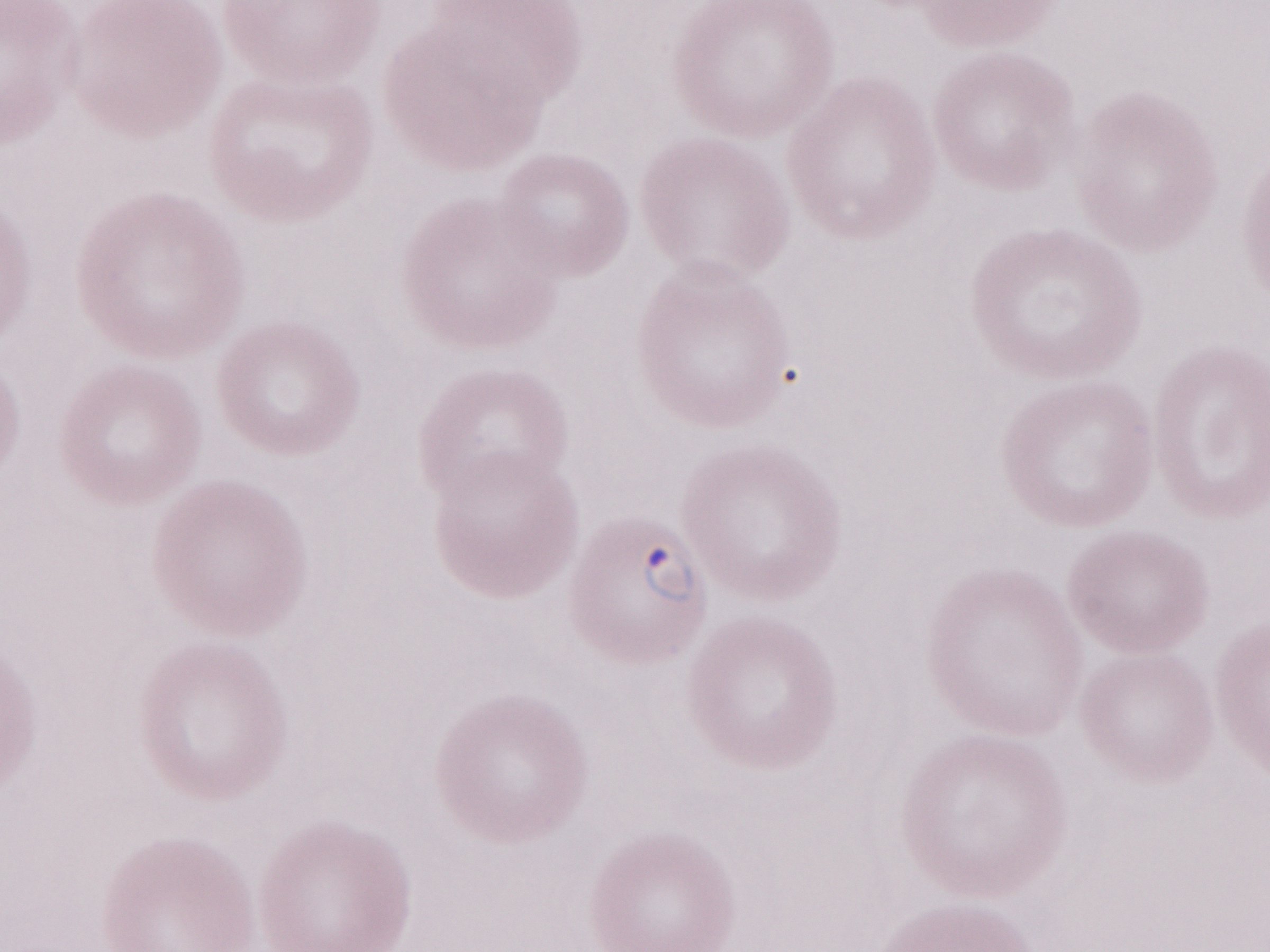 Thin peripheral-blood smear. Image is 1270×952 pixels. Magnification: 1,000x. One field of this slide. Patient diagnosis: malaria infection. Olympus BX43 microscope and DP73 digital camera. May-Grünwald-Giemsa-stained preparation.